Identify the parasite.
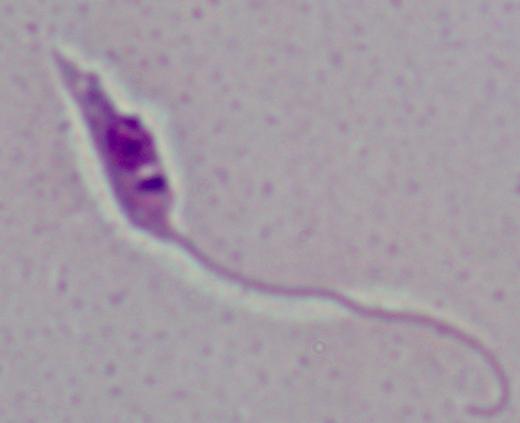

This is Leishmania.

modality = photomicrograph
magnification = 1000x